Locate every Plasmodium parasite.
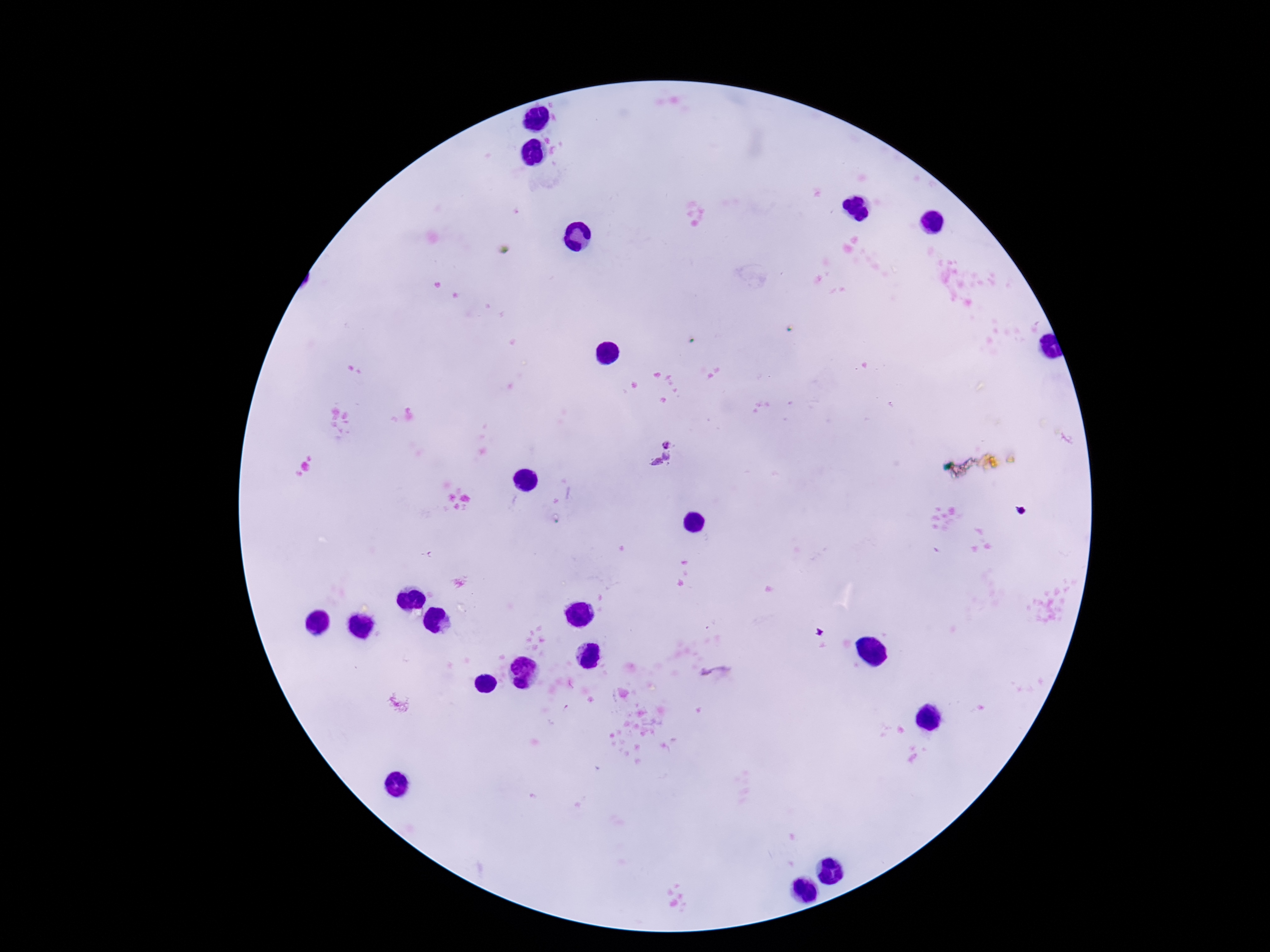

Approximate centers as (x, y) in pixels.
Plasmodium parasites: (664, 456), (716, 672).

patient malaria status = infected
preparation = thick blood film
stain = Giemsa
magnification = 100x
image size = 1270×952 pixels
field of view = one from this slide
capture = smartphone camera through the microscope eyepiece